Assess for Plasmodium parasites.
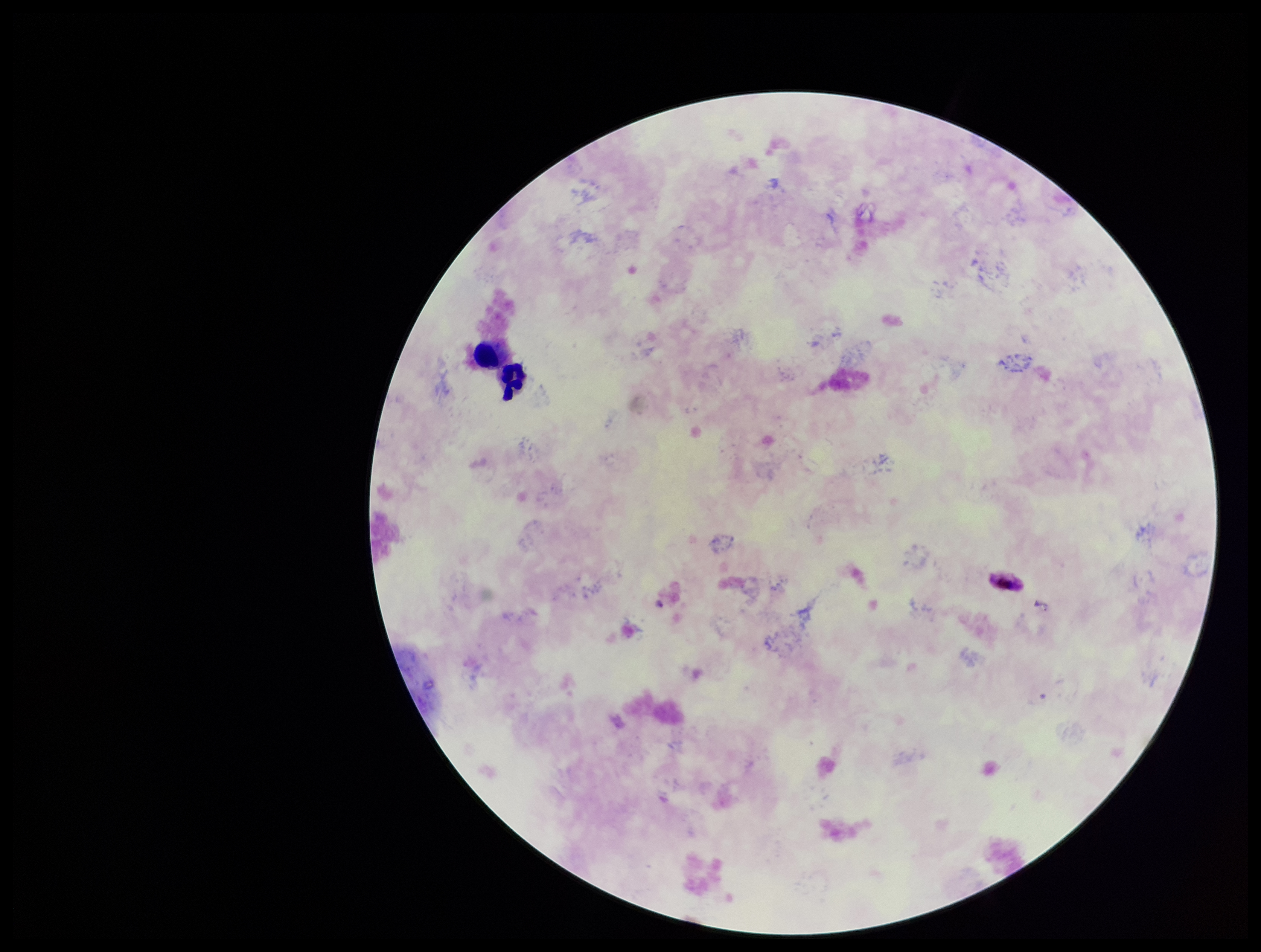
Identified.

species reported for this patient = Plasmodium falciparum
patient malaria status = positive
preparation = thick smear
parasite count = 1
capture = smartphone photograph through the microscope eyepiece
field of view = one from this slide
stain = Giemsa
leukocyte count = 2
image size = 1261×952 pixels